Comment on the morphology of the erythrocytes.
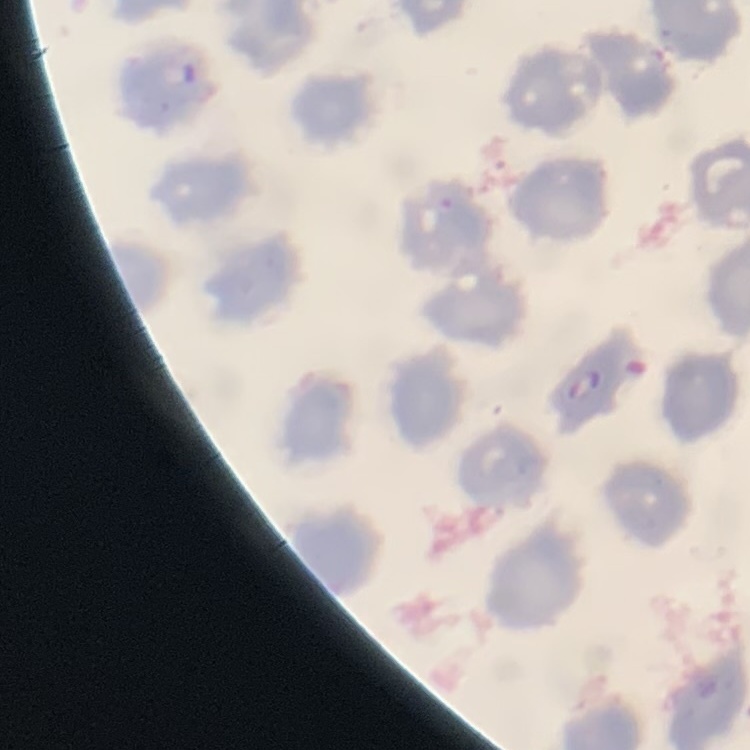
No rouleaux formation.

Summary:
  - Stain: Field's or Giemsa
  - Image type: one tile cut from a larger photomicrograph
  - Preparation: thin blood film